Identify the parasite.
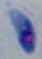

Toxoplasma gondii.

modality = photomicrograph
magnification = 1000x